State which parasite is depicted.
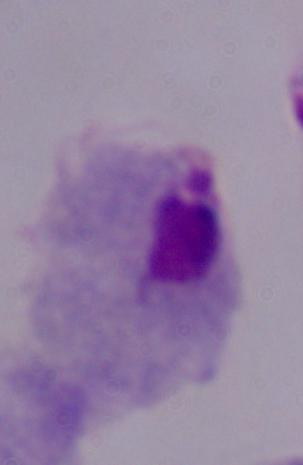

A trichomonad.

Micrograph. Captured at 1000x magnification.